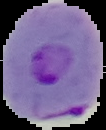 Malaria status: parasitized. The area outside the segmented cell region is set to black. Image is 106×130 pixels. From a thin blood film.